Report the malaria status of this cell.
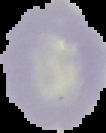

It is uninfected.

From a thin blood film. Image is 106×133 pixels. The area outside the segmented cell region is set to black.